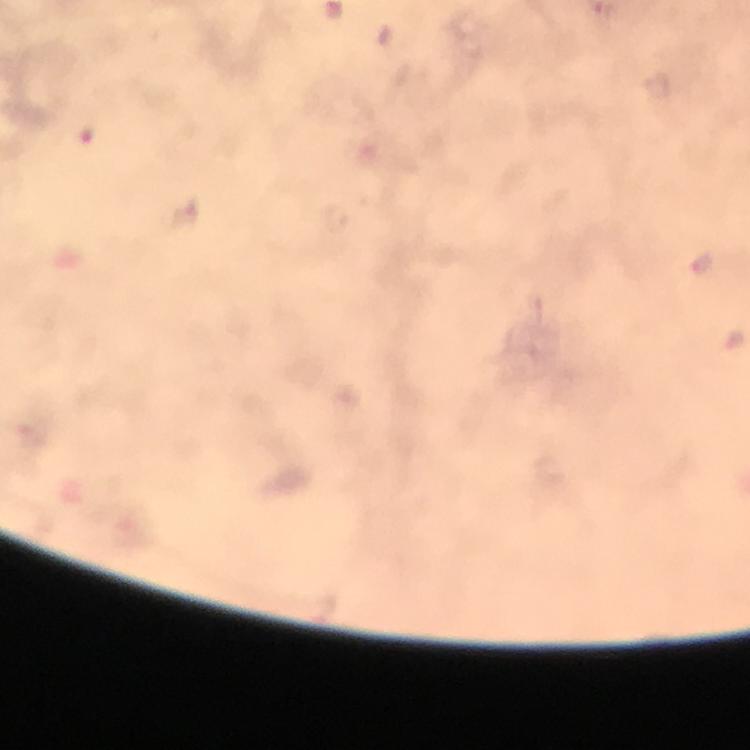

{
  "preparation": "thick smear",
  "malaria_parasite_locations": "approximate object centers, in pixels from the top-left corner: (x=658, y=87), (x=702, y=265)",
  "cropped_from": "one field of view",
  "image_size": "750×750 pixels",
  "magnification": "100x",
  "capture": "smartphone photograph through a microscope",
  "immersion_oil": "applied",
  "stain": "Giemsa",
  "context": "from a diagnostic examination for malaria"
}